Name the blood parasite species.
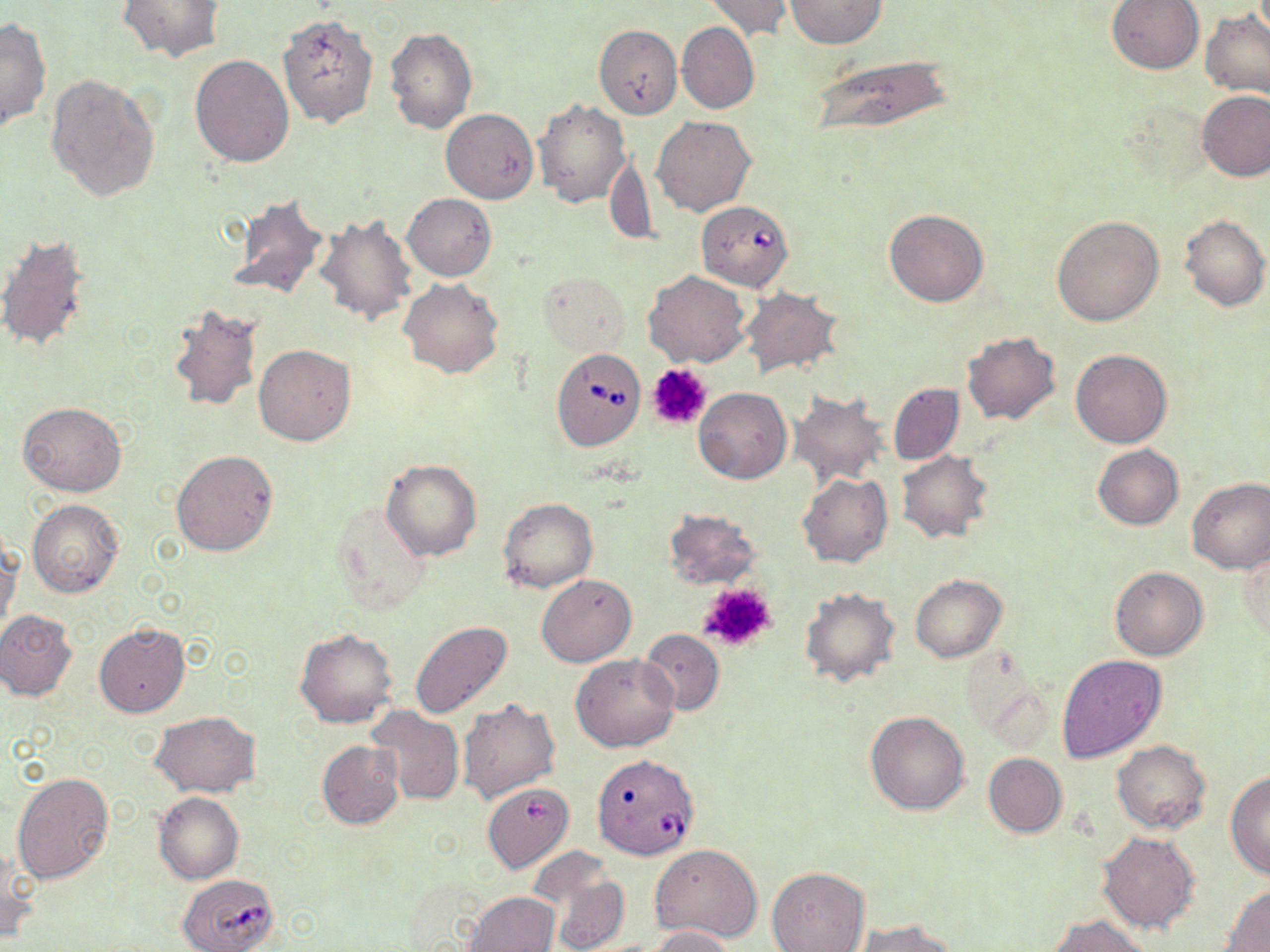

Babesia divergens.

{
  "field_of_view": "one of a larger specimen",
  "preparation": "thin blood smear",
  "platelet_locations": "approximate bounding boxes as [x1, y1, x2, y2] in pixels: [647, 363, 712, 430], [697, 582, 777, 654]",
  "image_size": "1270×952 pixels",
  "modality": "light microscopy",
  "uninfected_red_blood_cell_locations": "approximate bounding boxes as [x1, y1, x2, y2] in pixels: [703, 0, 794, 40], [785, 0, 888, 48], [1106, 0, 1203, 74], [117, 1, 226, 63], [1199, 8, 1270, 101], [278, 15, 377, 127], [1, 18, 50, 131], [676, 22, 759, 114], [594, 25, 683, 119], [384, 28, 477, 134], [809, 53, 956, 135], [190, 55, 294, 168], [46, 74, 161, 202], [1197, 90, 1269, 181], [534, 99, 629, 206], [440, 109, 538, 203], [652, 115, 756, 215], [607, 154, 657, 248], [225, 193, 331, 302], [402, 193, 496, 281], [885, 208, 990, 307], [315, 214, 417, 327], [1179, 214, 1270, 312], [1051, 215, 1164, 325], [0, 233, 93, 353], [644, 270, 751, 368], [538, 272, 629, 355], [399, 277, 504, 378], [741, 287, 843, 380], [166, 304, 263, 412], [962, 332, 1059, 424], [254, 343, 356, 445], [1071, 349, 1172, 448], [889, 382, 964, 465], [694, 387, 791, 484], [789, 393, 888, 486], [18, 402, 126, 496], [1093, 444, 1183, 530], [171, 451, 278, 556], [897, 451, 993, 543], [382, 460, 481, 560], [798, 472, 892, 568], [1186, 477, 1270, 574], [499, 498, 597, 591], [27, 499, 123, 598], [329, 499, 434, 616], [662, 509, 761, 589], [0, 539, 20, 638], [1238, 542, 1269, 643], [1110, 566, 1208, 660], [537, 574, 636, 666], [909, 575, 1005, 662], [800, 589, 899, 686], [1, 610, 77, 701], [95, 621, 190, 717], [409, 621, 514, 719], [294, 628, 397, 729], [641, 628, 724, 715], [1056, 653, 1166, 763], [570, 654, 679, 752], [458, 697, 560, 804], [368, 707, 464, 805], [865, 711, 970, 816], [151, 712, 257, 798], [318, 740, 403, 829], [1112, 741, 1212, 834], [983, 753, 1066, 836], [12, 771, 114, 884], [1225, 771, 1270, 880], [482, 782, 575, 874], [154, 793, 243, 884], [1098, 832, 1201, 935], [1, 843, 34, 946], [651, 844, 763, 942], [534, 854, 627, 952], [767, 867, 870, 952], [1220, 885, 1270, 950], [466, 892, 559, 952], [1049, 914, 1154, 952], [855, 920, 958, 952], [645, 926, 734, 952]",
  "babesia_divergens_infected_red_blood_cell_locations": "approximate bounding boxes as [x1, y1, x2, y2] in pixels: [696, 200, 795, 291], [551, 348, 645, 451], [594, 761, 697, 863], [178, 875, 283, 952]",
  "stain": "May-Grünwald-Giemsa",
  "magnification": "1000x"
}